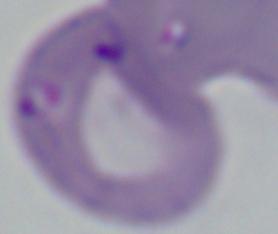

modality = photomicrograph
magnification = 1000x
identification = Babesia